Point out each malaria parasite.
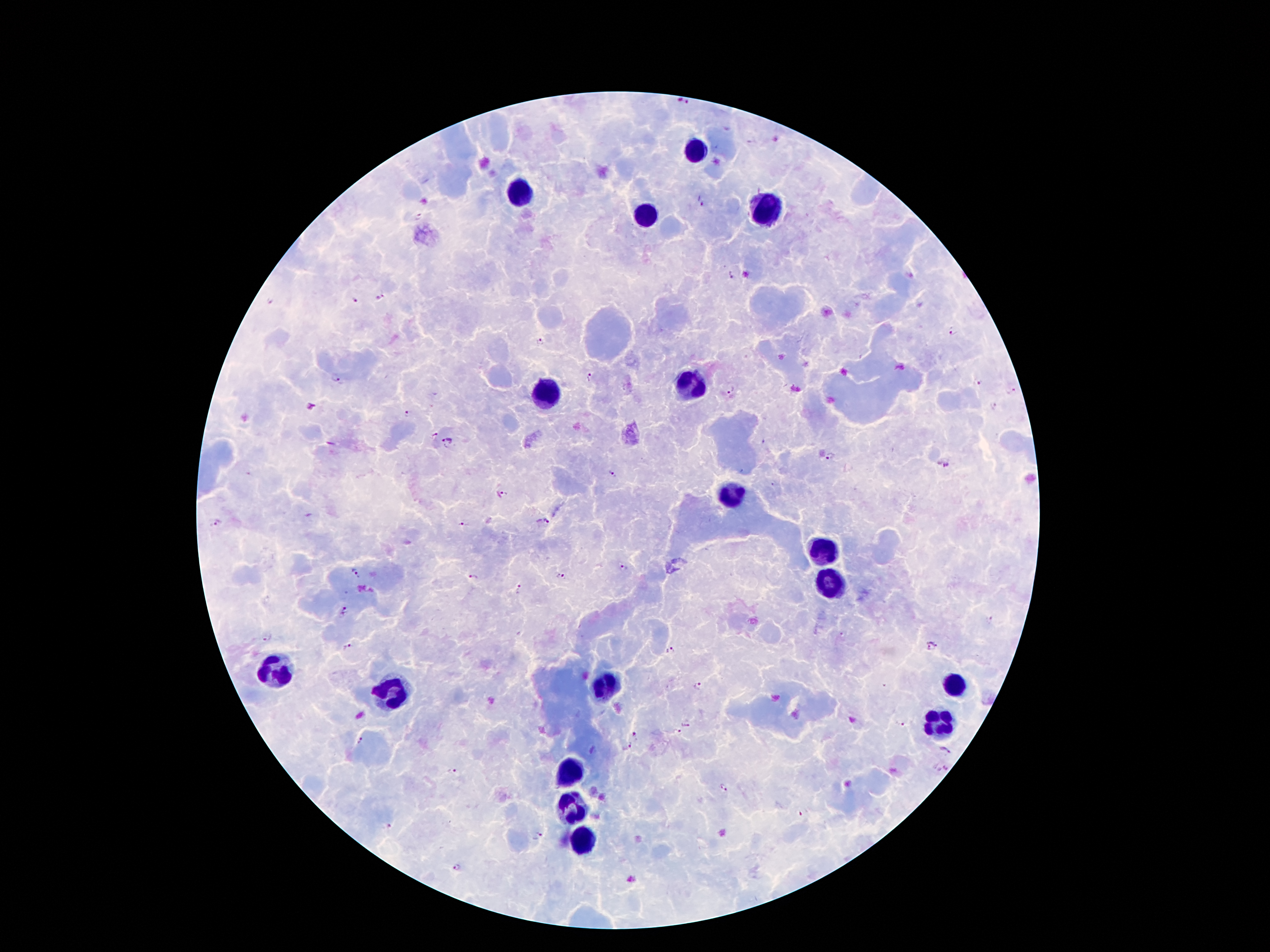
Approximate centers as [x, y] in pixels.
Malaria parasites: [682, 103], [730, 276], [379, 297], [354, 302], [954, 332], [540, 340], [591, 376], [336, 378], [978, 383], [730, 389], [1011, 390], [993, 405], [310, 407], [406, 413], [447, 441], [831, 458], [946, 466], [611, 474], [504, 492], [548, 522], [217, 523], [464, 525], [623, 568], [356, 573], [561, 576], [473, 578], [519, 589], [344, 611], [989, 619], [267, 637], [932, 646], [346, 647], [669, 651], [698, 687], [685, 722], [899, 723], [676, 732], [634, 734], [362, 742], [624, 745], [946, 749], [943, 766], [452, 772], [723, 788], [390, 827], [537, 837], [457, 868].

leukocyte locations = [697, 145], [521, 189], [645, 217], [771, 217], [693, 383], [551, 393], [733, 493], [829, 549], [833, 583], [275, 669], [953, 681], [603, 685], [391, 695], [939, 725], [573, 775], [571, 801], [581, 843]
magnification = 100x
image size = 1270×952 pixels
capture = smartphone through the microscope eyepiece
preparation = thick blood smear
stain = Giemsa
patient malaria status = positive for Plasmodium falciparum
field of view = single